Report the malaria status of this cell.
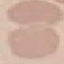
Uninfected.

Giemsa stain. Automatically extracted cell patch, resized to 64 × 64 pixels. Photographed with a smartphone camera at the microscope eyepiece. Thin smear of blood.